Evaluate for malaria.
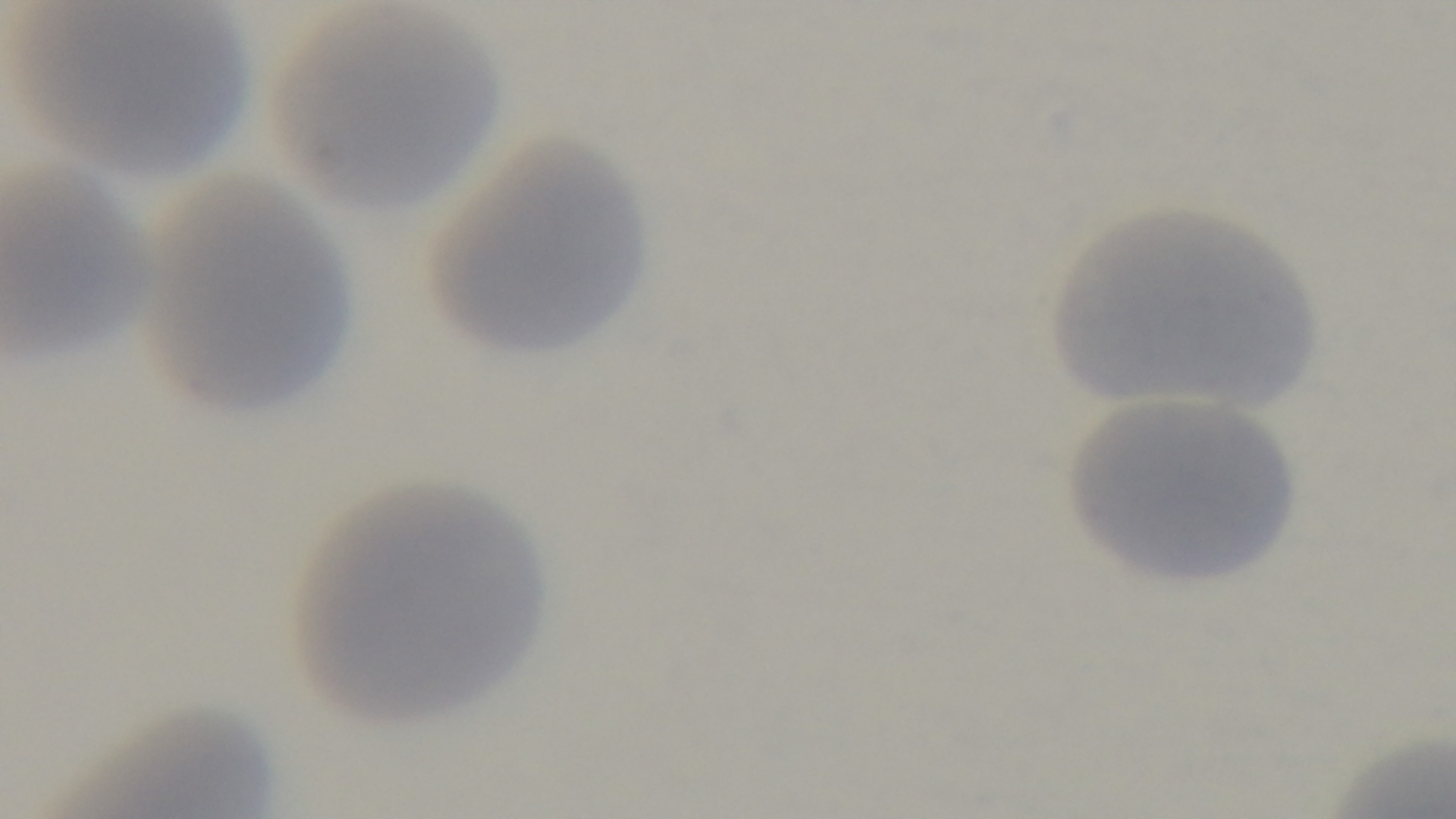

Uninfected.

Summary:
  - Preparation: thin blood film
  - Field of view: single
  - Modality: light microscopy
  - Objective: 100x oil immersion
  - Stain: Giemsa
  - Capture: mounted 4K digital camera